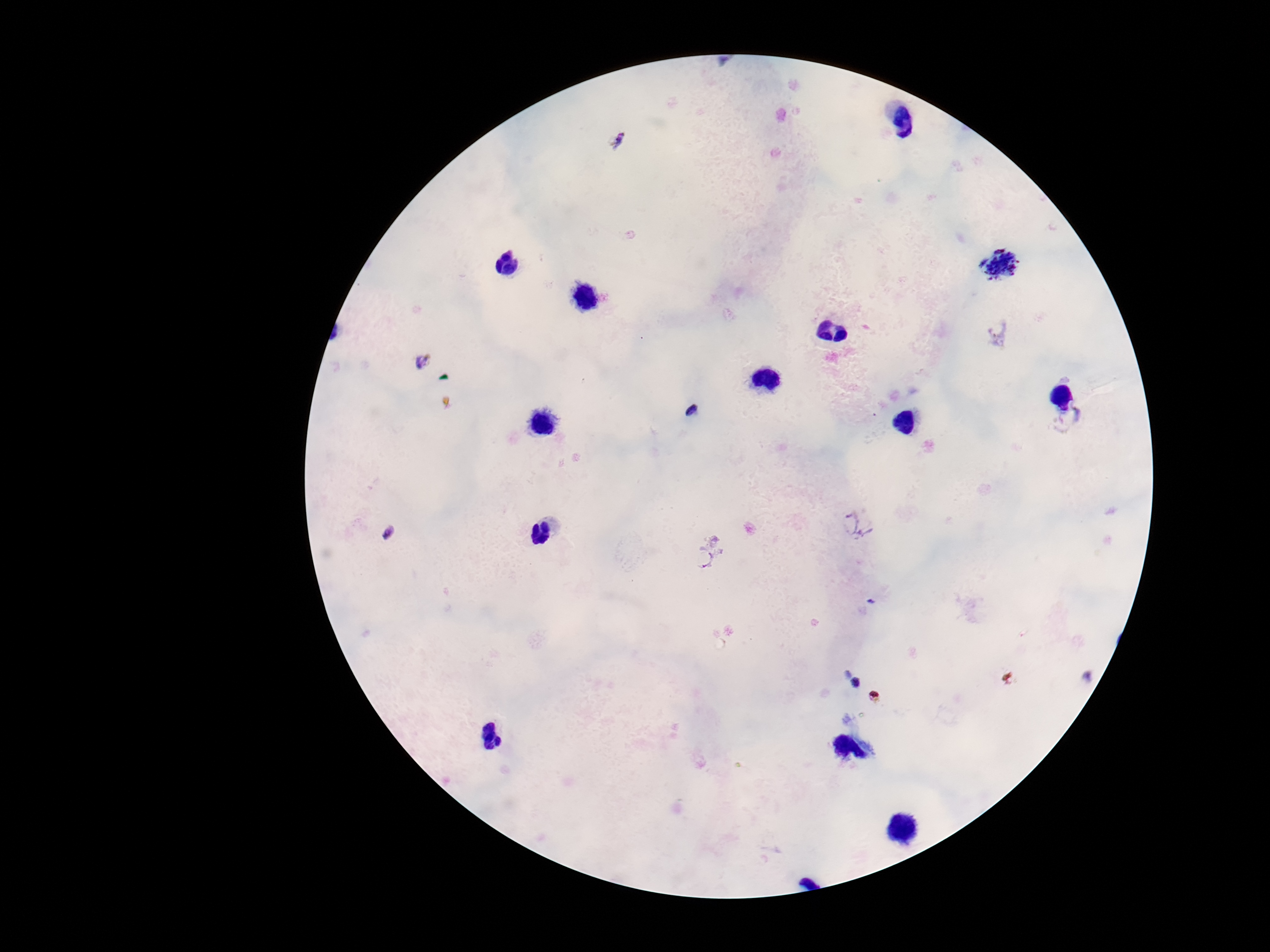
Plasmodium parasite locations = approximate centers as (x, y) in pixels: (615, 141), (1002, 265), (998, 332), (421, 360), (689, 411), (1068, 421), (857, 524), (389, 533), (707, 554), (856, 683)
stain = Giemsa
patient malaria status = infected
image size = 1270×952 pixels
capture = smartphone camera through the microscope eyepiece
field of view = single
preparation = thick blood film
magnification = 100x